State which cell type is depicted.
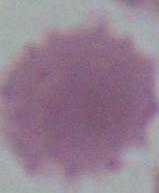
An erythrocyte.

Summary:
  - Modality: micrograph
  - Magnification: 1000x